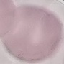

malaria_status: uninfected
preparation: thin blood film
image_type: cell patch, automatically extracted from a larger field of view and resized to 64 × 64 pixels
stain: Giemsa
capture: smartphone camera at the microscope eyepiece